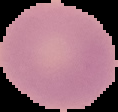
Malaria status: uninfected. Cell region segmented out of the field of view; the surrounding area is masked to black. Image is 118×112 pixels. From a thin blood film.